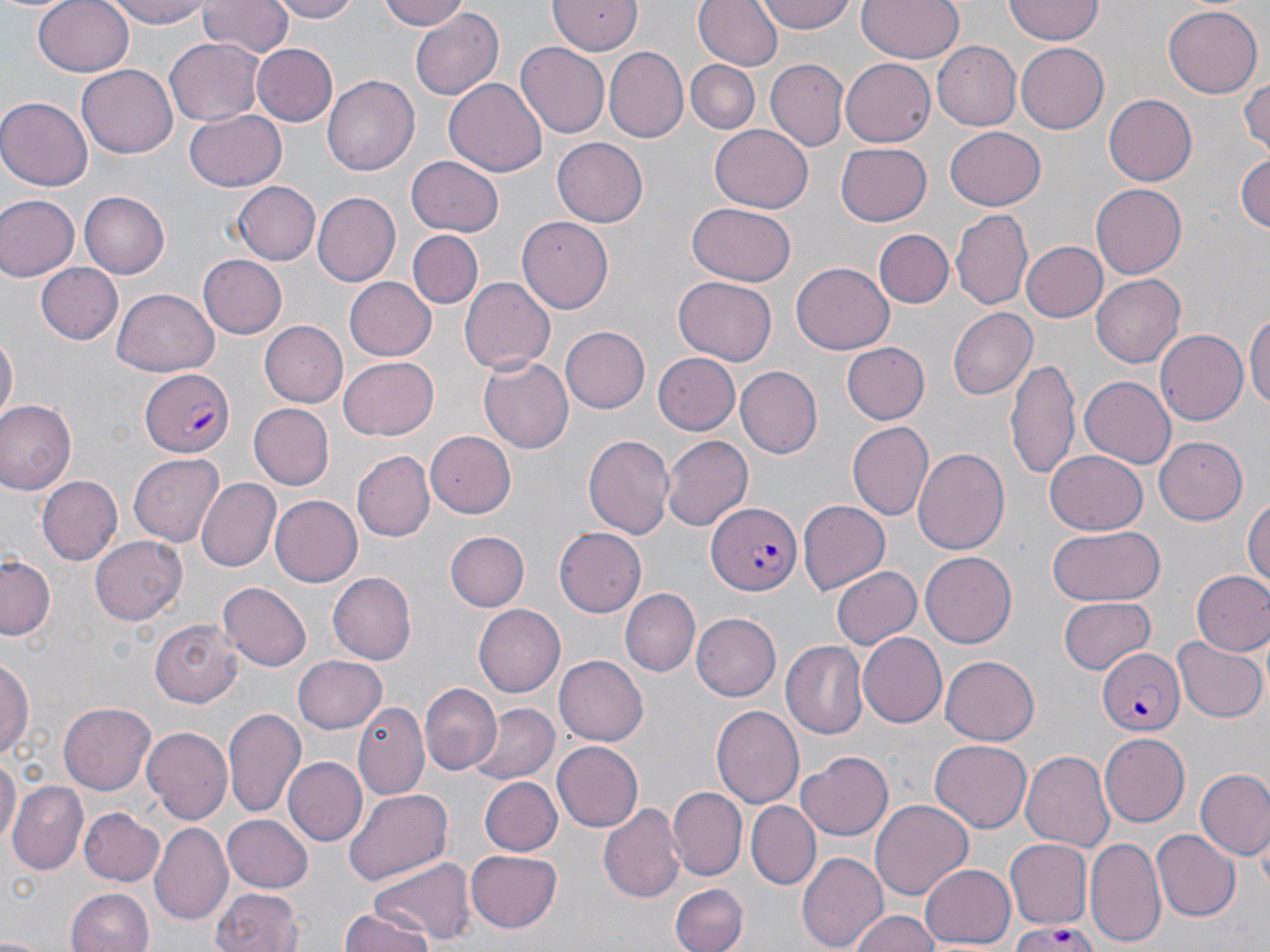

Summary:
  - Coordinate format: approximate bounding boxes as [x1, y1, x2, y2] in pixels
  - Uninfected red blood cell locations: [35, 0, 134, 75], [106, 0, 216, 29], [267, 0, 359, 23], [375, 0, 472, 31], [548, 0, 645, 56], [694, 0, 782, 71], [758, 0, 855, 34], [857, 0, 963, 64], [197, 1, 292, 60], [1005, 1, 1105, 44], [1162, 5, 1263, 98], [410, 7, 505, 100], [163, 39, 265, 125], [931, 41, 1020, 131], [251, 42, 337, 126], [1016, 42, 1109, 133], [515, 43, 610, 138], [603, 46, 686, 142], [841, 57, 938, 147], [766, 58, 849, 152], [685, 60, 759, 134], [77, 65, 179, 158], [1240, 74, 1270, 158], [322, 75, 420, 175], [444, 78, 546, 177], [1103, 94, 1197, 186], [0, 97, 92, 189], [184, 109, 287, 193], [707, 125, 814, 214], [944, 127, 1044, 210], [551, 138, 648, 228], [835, 144, 932, 227], [1234, 152, 1270, 236], [407, 156, 504, 235], [233, 180, 321, 265], [1090, 184, 1186, 279], [79, 192, 171, 279], [311, 193, 399, 286], [0, 195, 76, 280], [687, 201, 795, 285], [952, 210, 1033, 310], [516, 217, 613, 313], [874, 227, 953, 307], [410, 229, 482, 307], [1021, 241, 1107, 323], [198, 255, 287, 339], [793, 261, 896, 355], [36, 265, 121, 344], [1092, 273, 1184, 366], [674, 276, 776, 365], [345, 277, 436, 361], [460, 277, 557, 374], [111, 286, 219, 375], [1246, 307, 1270, 418], [947, 308, 1036, 400], [260, 322, 347, 407], [561, 328, 649, 414], [1154, 329, 1246, 427], [1, 334, 17, 426], [842, 342, 929, 425], [652, 352, 740, 433], [480, 355, 573, 452], [1007, 355, 1081, 485], [340, 356, 439, 439], [735, 368, 822, 457], [1079, 376, 1174, 470], [1, 400, 77, 494], [249, 404, 333, 490], [847, 420, 933, 521], [583, 431, 675, 543], [424, 432, 515, 519], [662, 436, 753, 530], [1153, 437, 1246, 525], [912, 447, 1009, 559], [353, 451, 434, 541], [1044, 452, 1147, 533], [129, 453, 225, 546], [37, 476, 123, 565], [196, 478, 279, 571], [1246, 494, 1270, 596], [267, 495, 362, 586], [798, 501, 889, 594], [1047, 525, 1165, 607], [553, 527, 645, 617], [443, 530, 527, 612], [90, 536, 186, 623], [921, 552, 1018, 647], [1, 554, 58, 641], [833, 566, 921, 650], [1192, 570, 1270, 655], [327, 572, 417, 665], [219, 581, 310, 671], [618, 586, 700, 674], [1059, 595, 1156, 673], [472, 604, 564, 697], [691, 612, 781, 701], [150, 617, 242, 707], [857, 633, 945, 728], [1173, 636, 1266, 723], [783, 640, 871, 738], [555, 654, 650, 745], [940, 654, 1040, 744], [293, 655, 387, 735], [1, 656, 35, 759], [309, 660, 417, 773], [421, 683, 501, 775], [353, 700, 428, 798], [58, 702, 156, 794], [470, 702, 559, 785], [710, 703, 803, 808], [224, 707, 306, 819], [143, 727, 232, 826], [1101, 734, 1190, 826], [927, 740, 1031, 833], [552, 741, 644, 834], [798, 750, 893, 839], [1022, 750, 1115, 855], [0, 752, 19, 855], [283, 756, 367, 846], [1195, 768, 1270, 863], [478, 776, 561, 857], [9, 783, 89, 873], [668, 786, 747, 881], [343, 788, 454, 885], [869, 800, 972, 901], [748, 801, 820, 890], [599, 802, 684, 905], [79, 806, 164, 884], [222, 815, 313, 893], [152, 822, 231, 923], [1154, 829, 1240, 920], [1086, 836, 1164, 948], [1004, 839, 1090, 929], [465, 849, 564, 933], [798, 850, 887, 952], [366, 857, 477, 946], [919, 862, 1017, 948], [671, 884, 747, 952], [66, 887, 155, 952], [211, 887, 307, 952], [848, 910, 946, 952], [339, 911, 437, 952], [0, 932, 50, 952]
  - Plasmodium falciparum-infected red blood cell locations: [140, 369, 235, 456], [707, 502, 800, 597], [1096, 647, 1185, 735], [1009, 924, 1102, 952]
  - Slide-level diagnosis: Plasmodium falciparum
  - Image size: 1270×952 pixels
  - Preparation: thin blood smear
  - Stain: May-Grünwald-Giemsa
  - Field of view: one of a larger specimen
  - Magnification: 1000x
  - Modality: optical microscopy